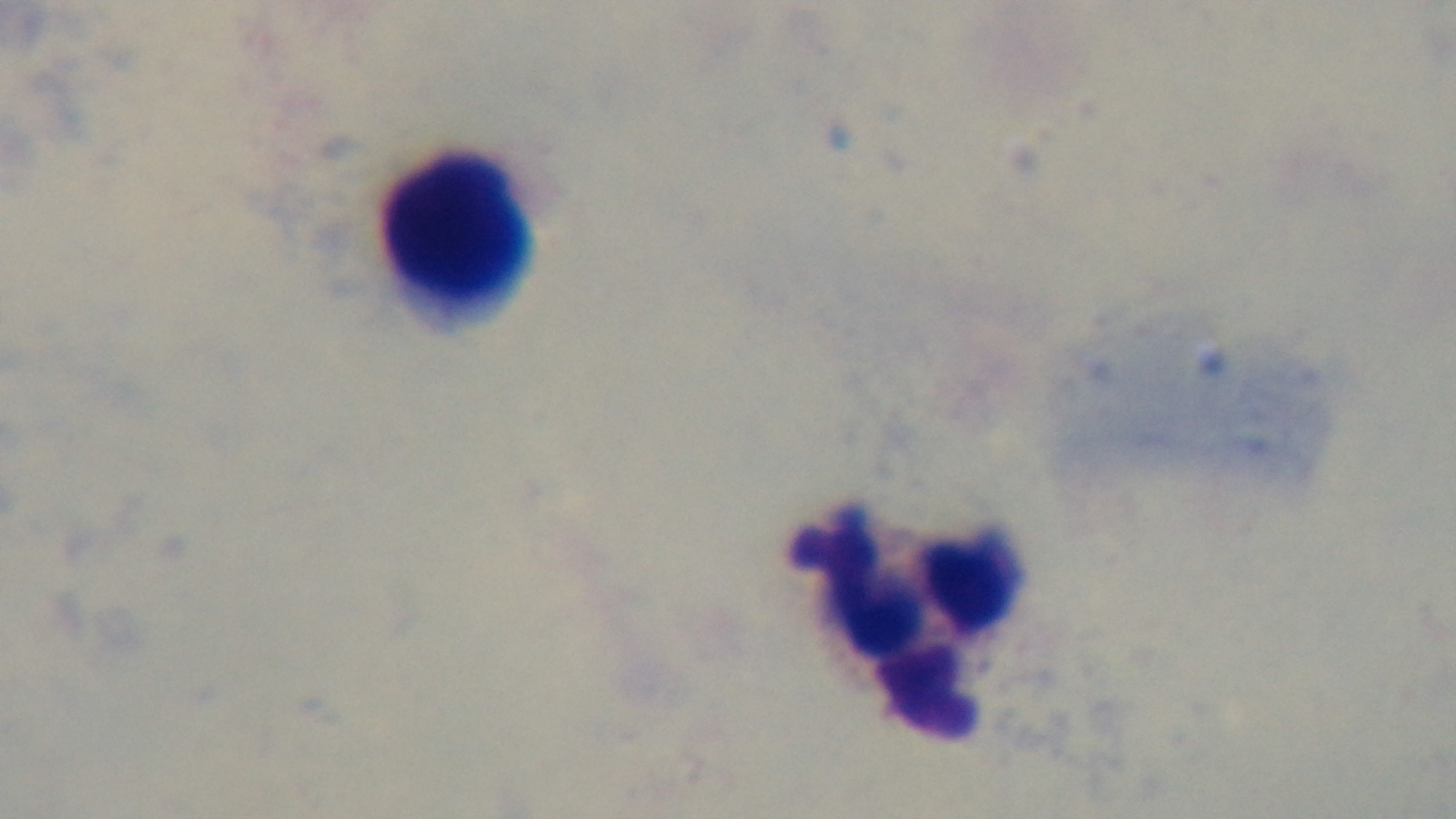
modality: light microscopy
preparation: thick blood film
field_of_view: single
stain: Giemsa
malaria_status: negative
objective: 100x oil immersion
capture: mounted 4K digital camera